Describe the morphology of the erythrocytes.
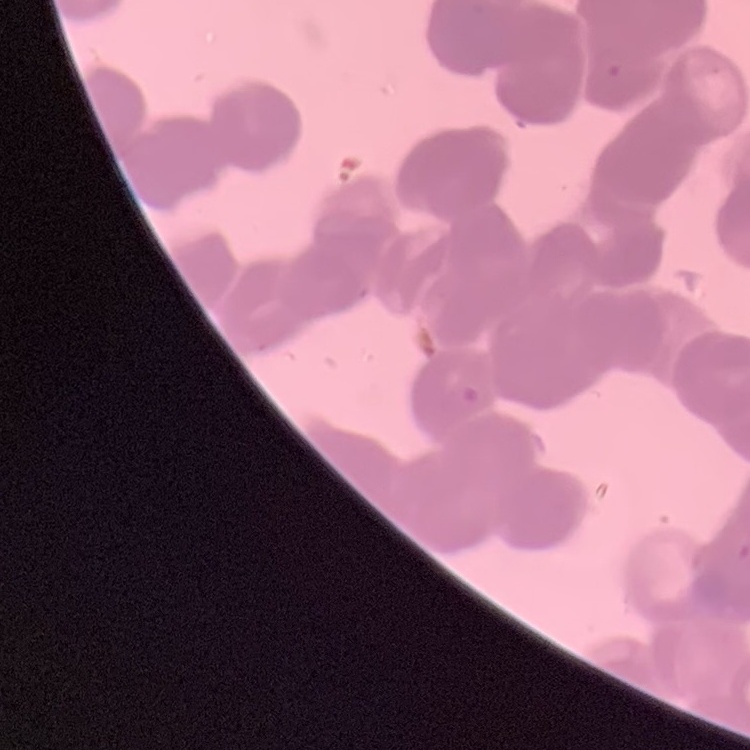

Rouleaux formation.

Summary:
  - Image type: one tile cut from a larger photomicrograph
  - Stain: Field's or Giemsa
  - Preparation: thin blood smear